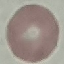
Result: negative for malaria parasites. Giemsa-stained preparation. Photographed with a smartphone camera at the microscope eyepiece. Thin blood smear. Cell patch, automatically extracted from a larger field of view and resized to 64 × 64 pixels.